Assess this cell for malaria.
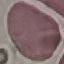

Uninfected.

Photographed with a smartphone camera at the microscope eyepiece. Giemsa stain. Thin smear of blood. Cell patch, automatically extracted from a larger field of view and resized to 64 × 64 pixels.